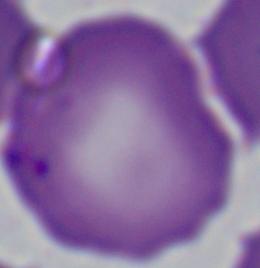

Summary:
  - Identification: Babesia
  - Magnification: 1000x
  - Modality: micrograph